Locate every malaria parasite and every leukocyte.
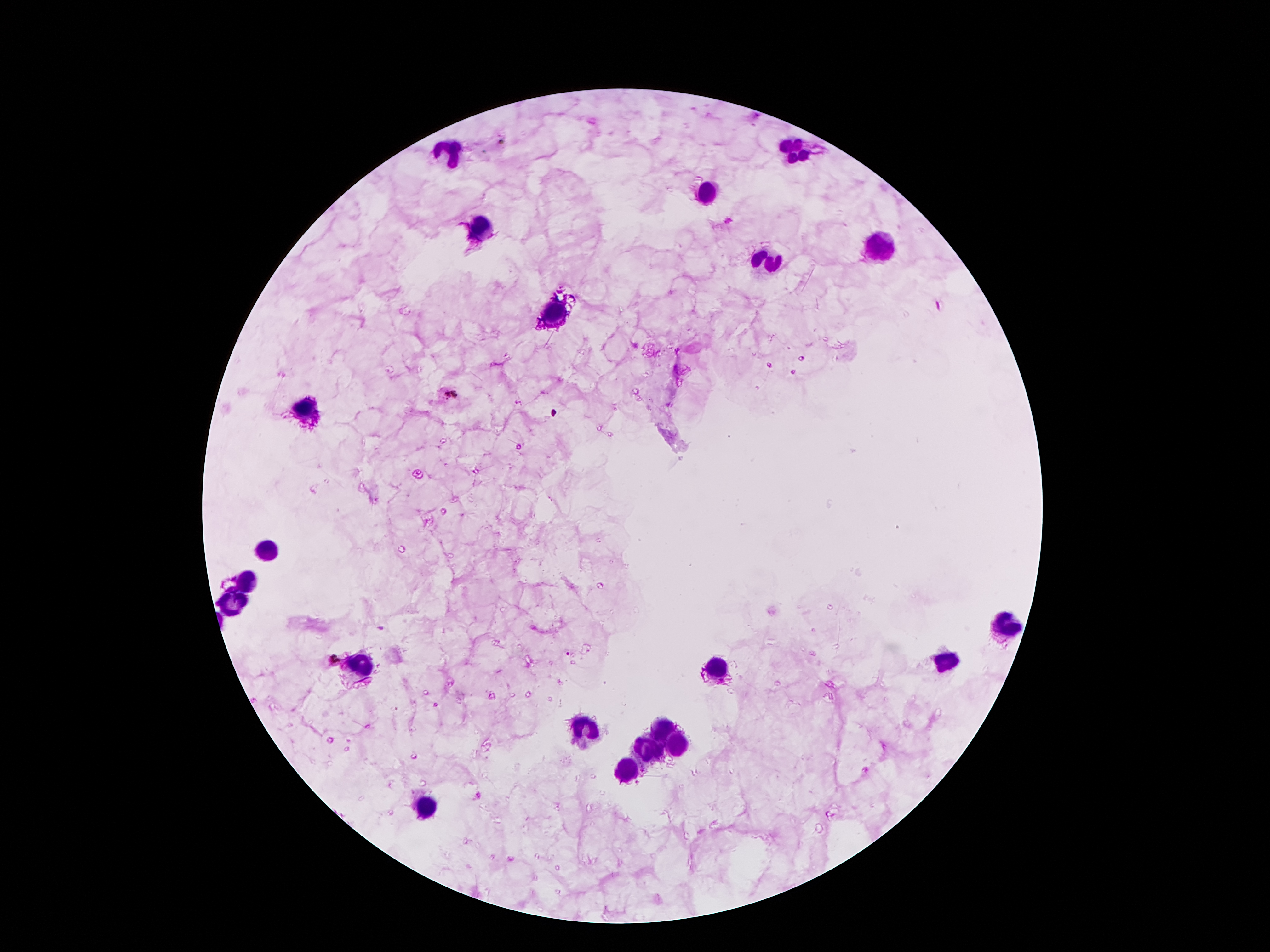

Approximate centers as (x, y) in pixels.
Malaria parasites: (940, 306), (555, 413), (566, 652), (332, 659).
Leukocytes: (445, 149), (794, 151), (706, 193), (475, 229), (878, 246), (766, 260), (554, 313), (309, 411), (269, 546), (251, 578), (237, 601), (1001, 625), (942, 660), (715, 662), (360, 664), (663, 727), (587, 730), (675, 744), (652, 751), (629, 769), (427, 807).

Photographed through the microscope eyepiece with a smartphone camera. Giemsa-stained preparation. One field from this slide. Thick blood film. 100x magnification. Image is 1270×952 pixels. Patient malaria status: positive for Plasmodium falciparum.